Assess this cell for malaria.
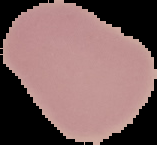
Uninfected.

Image is 157×145 pixels. From a thin blood smear. The area outside the segmented cell region is set to black.